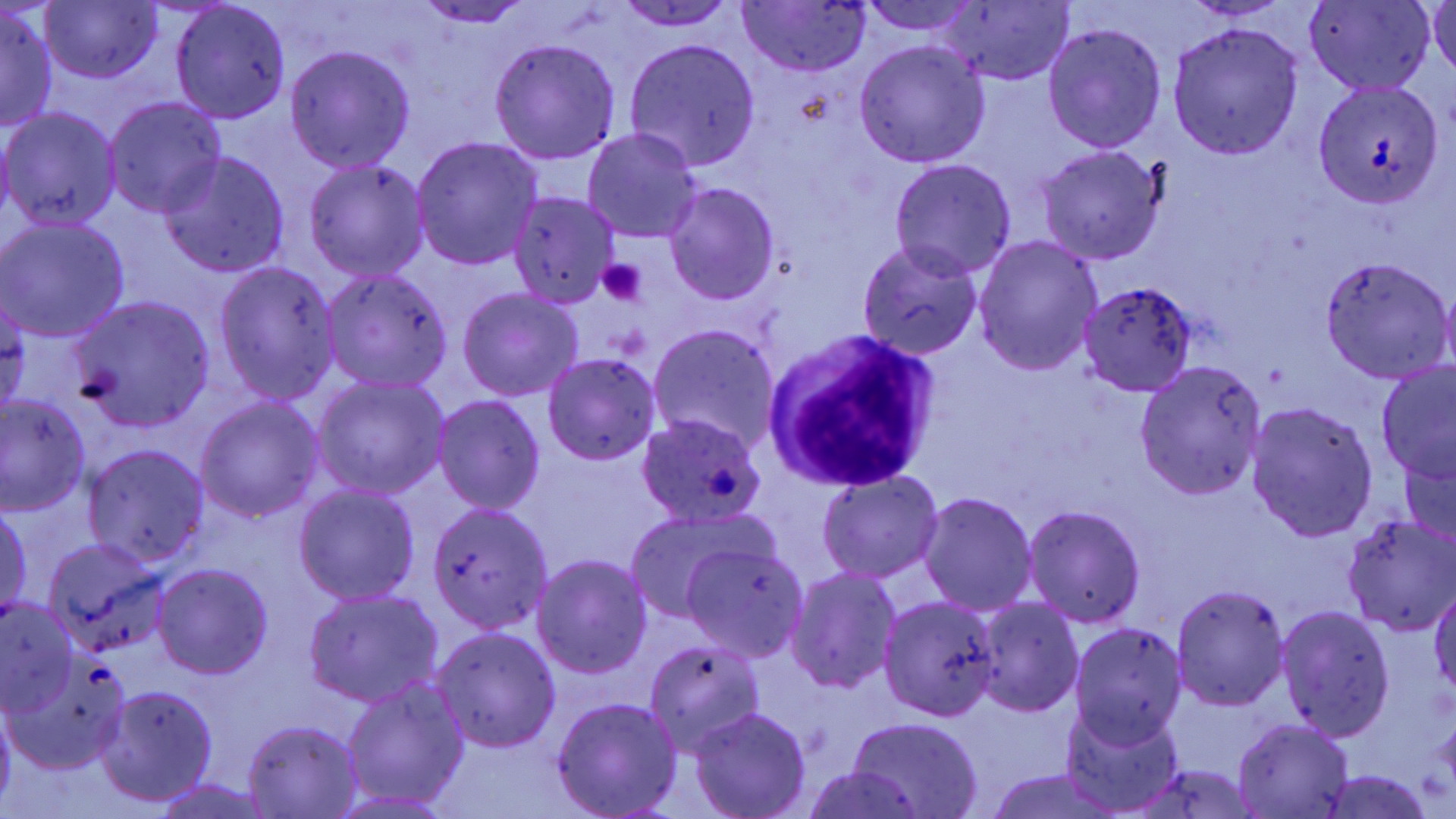
slide-level diagnosis = Plasmodium ovale
uninfected red blood cell locations = approximate bounding boxes as named x1/y1/x2/y2 corners in pixels: (x1=40, y1=0, x2=163, y2=84), (x1=1427, y1=0, x2=1455, y2=77), (x1=413, y1=1, x2=535, y2=28), (x1=614, y1=1, x2=736, y2=30), (x1=860, y1=2, x2=982, y2=37), (x1=1305, y1=2, x2=1435, y2=93), (x1=736, y1=3, x2=872, y2=75), (x1=938, y1=3, x2=1076, y2=84), (x1=1, y1=4, x2=57, y2=135), (x1=170, y1=4, x2=292, y2=122), (x1=1043, y1=22, x2=1166, y2=153), (x1=1168, y1=22, x2=1303, y2=158), (x1=624, y1=38, x2=762, y2=171), (x1=488, y1=39, x2=620, y2=164), (x1=854, y1=41, x2=990, y2=168), (x1=284, y1=45, x2=416, y2=173), (x1=1311, y1=78, x2=1450, y2=211), (x1=104, y1=96, x2=228, y2=217), (x1=2, y1=106, x2=121, y2=232), (x1=581, y1=130, x2=704, y2=244), (x1=411, y1=137, x2=543, y2=269), (x1=1036, y1=144, x2=1166, y2=264), (x1=159, y1=152, x2=289, y2=279), (x1=304, y1=158, x2=429, y2=283), (x1=888, y1=159, x2=1016, y2=280), (x1=663, y1=181, x2=781, y2=305), (x1=509, y1=191, x2=620, y2=307), (x1=0, y1=216, x2=130, y2=342), (x1=973, y1=235, x2=1104, y2=378), (x1=856, y1=243, x2=984, y2=361), (x1=1321, y1=256, x2=1454, y2=382), (x1=213, y1=261, x2=342, y2=405), (x1=321, y1=269, x2=456, y2=393), (x1=1080, y1=280, x2=1198, y2=398), (x1=1440, y1=285, x2=1456, y2=378), (x1=456, y1=289, x2=584, y2=401), (x1=0, y1=293, x2=31, y2=417), (x1=73, y1=298, x2=214, y2=431), (x1=648, y1=324, x2=780, y2=454), (x1=542, y1=353, x2=662, y2=464), (x1=1136, y1=359, x2=1266, y2=500), (x1=1375, y1=361, x2=1455, y2=484), (x1=310, y1=374, x2=450, y2=500), (x1=1, y1=393, x2=92, y2=514), (x1=194, y1=395, x2=325, y2=522), (x1=433, y1=396, x2=546, y2=512), (x1=1245, y1=401, x2=1378, y2=543), (x1=634, y1=413, x2=765, y2=528), (x1=81, y1=444, x2=210, y2=568), (x1=1400, y1=450, x2=1455, y2=548), (x1=817, y1=471, x2=944, y2=583), (x1=293, y1=483, x2=421, y2=606), (x1=917, y1=491, x2=1038, y2=617), (x1=427, y1=500, x2=555, y2=635), (x1=1023, y1=503, x2=1147, y2=628), (x1=1, y1=505, x2=32, y2=623), (x1=623, y1=511, x2=769, y2=630), (x1=1342, y1=515, x2=1456, y2=634), (x1=44, y1=538, x2=169, y2=657), (x1=681, y1=541, x2=806, y2=662), (x1=532, y1=555, x2=652, y2=680), (x1=153, y1=563, x2=274, y2=681), (x1=786, y1=567, x2=902, y2=694), (x1=1170, y1=584, x2=1291, y2=709), (x1=1430, y1=584, x2=1456, y2=695), (x1=303, y1=588, x2=443, y2=708), (x1=879, y1=596, x2=1002, y2=721), (x1=973, y1=599, x2=1082, y2=720), (x1=1, y1=602, x2=81, y2=713), (x1=1277, y1=604, x2=1397, y2=743), (x1=1070, y1=622, x2=1186, y2=746), (x1=432, y1=626, x2=562, y2=754), (x1=643, y1=640, x2=766, y2=757), (x1=2, y1=653, x2=132, y2=774), (x1=343, y1=679, x2=469, y2=807), (x1=95, y1=687, x2=217, y2=806), (x1=552, y1=696, x2=682, y2=818), (x1=0, y1=697, x2=17, y2=812), (x1=1061, y1=704, x2=1183, y2=816), (x1=690, y1=706, x2=812, y2=819), (x1=848, y1=716, x2=982, y2=819), (x1=241, y1=719, x2=364, y2=817), (x1=1233, y1=720, x2=1355, y2=816), (x1=1131, y1=764, x2=1262, y2=819), (x1=801, y1=765, x2=928, y2=819), (x1=982, y1=769, x2=1128, y2=819), (x1=1319, y1=771, x2=1440, y2=817), (x1=150, y1=779, x2=276, y2=818)
platelet locations = approximate bounding boxes as named x1/y1/x2/y2 corners in pixels: (x1=597, y1=258, x2=648, y2=306)
white blood cell locations = approximate bounding boxes as named x1/y1/x2/y2 corners in pixels: (x1=765, y1=326, x2=935, y2=490)
modality = light microscopy
stain = May-Grünwald-Giemsa
preparation = thin blood film
field of view = one of a larger specimen
image size = 1456×819 pixels
magnification = 1000x